Point out each Plasmodium parasite.
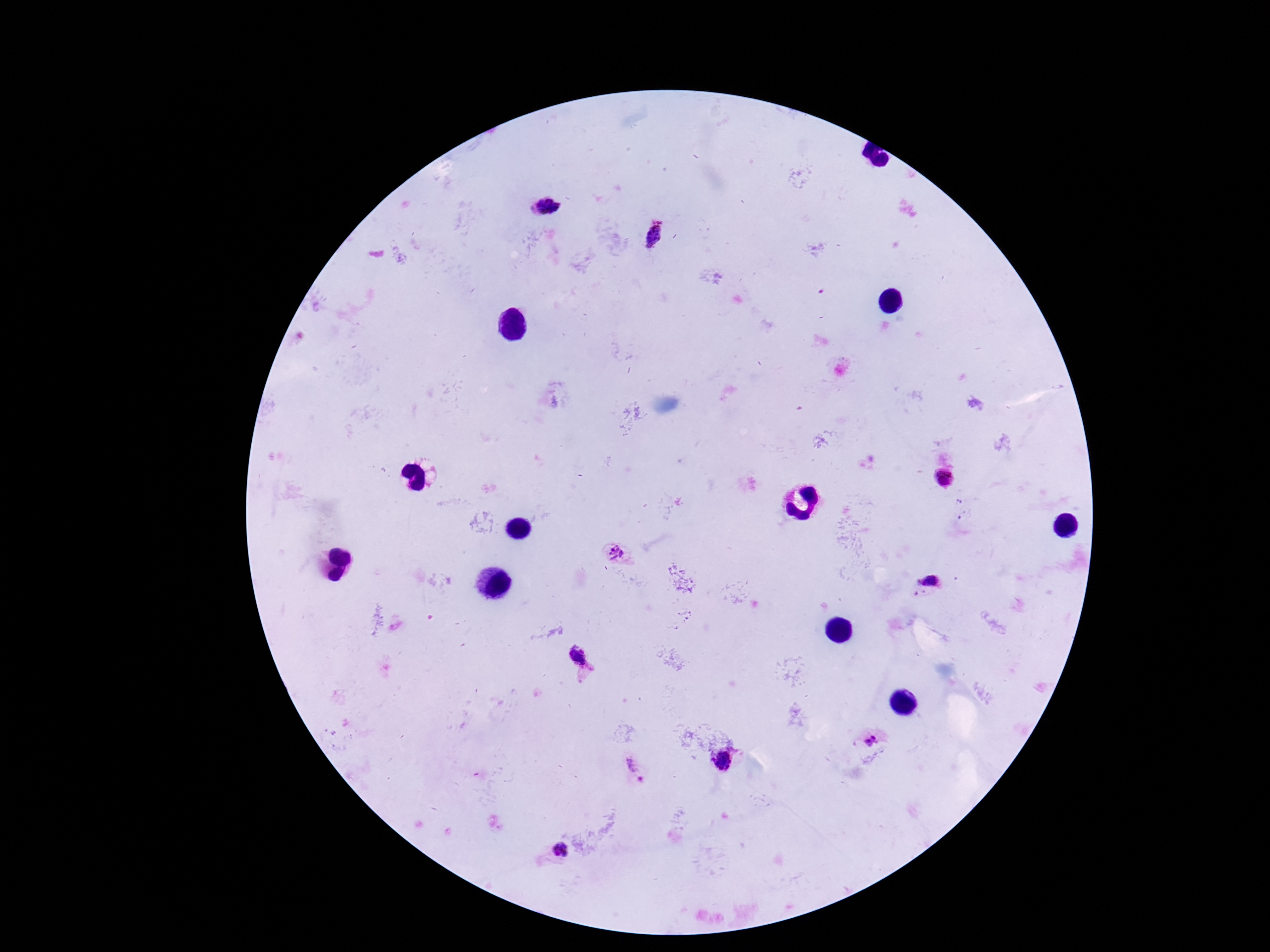
Approximate centers as (x, y) in pixels.
Plasmodium parasites: (547, 206), (653, 235), (943, 477), (617, 553), (928, 581), (579, 659), (872, 741), (723, 761), (637, 770), (557, 852).

magnification = 100x
patient malaria status = infected
preparation = thick blood smear
capture = smartphone camera through the microscope eyepiece
field of view = single
stain = Giemsa
image size = 1270×952 pixels